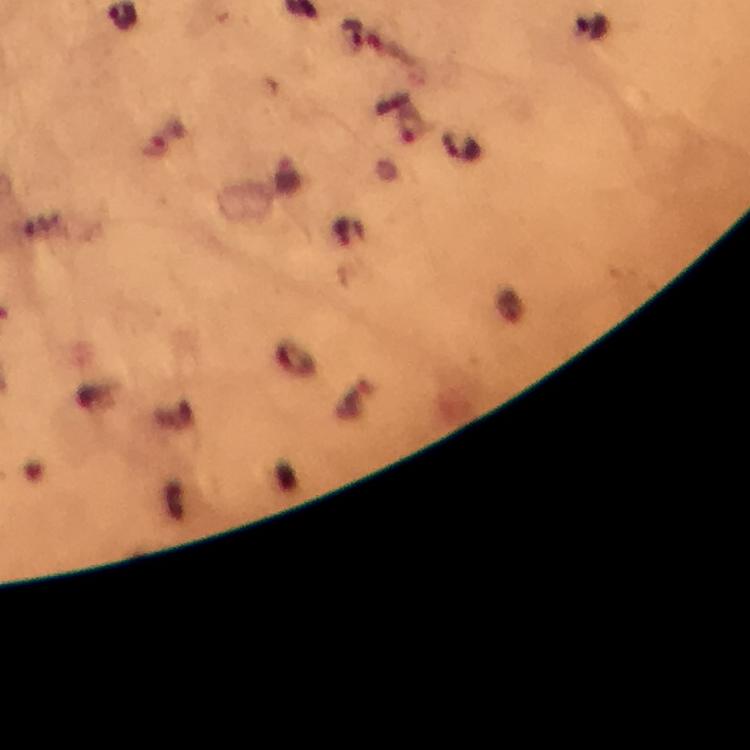

Approximate centers as (x, y) in pixels. Plasmodium parasite locations: (461, 145). Photographed through the microscope with a smartphone camera. Immersion oil applied. Thick blood film. Giemsa stain. Image is 750×750 pixels. At 100x magnification. From a malaria diagnostic workup. A crop from one field of view.